Outline each uninfected red blood cell.
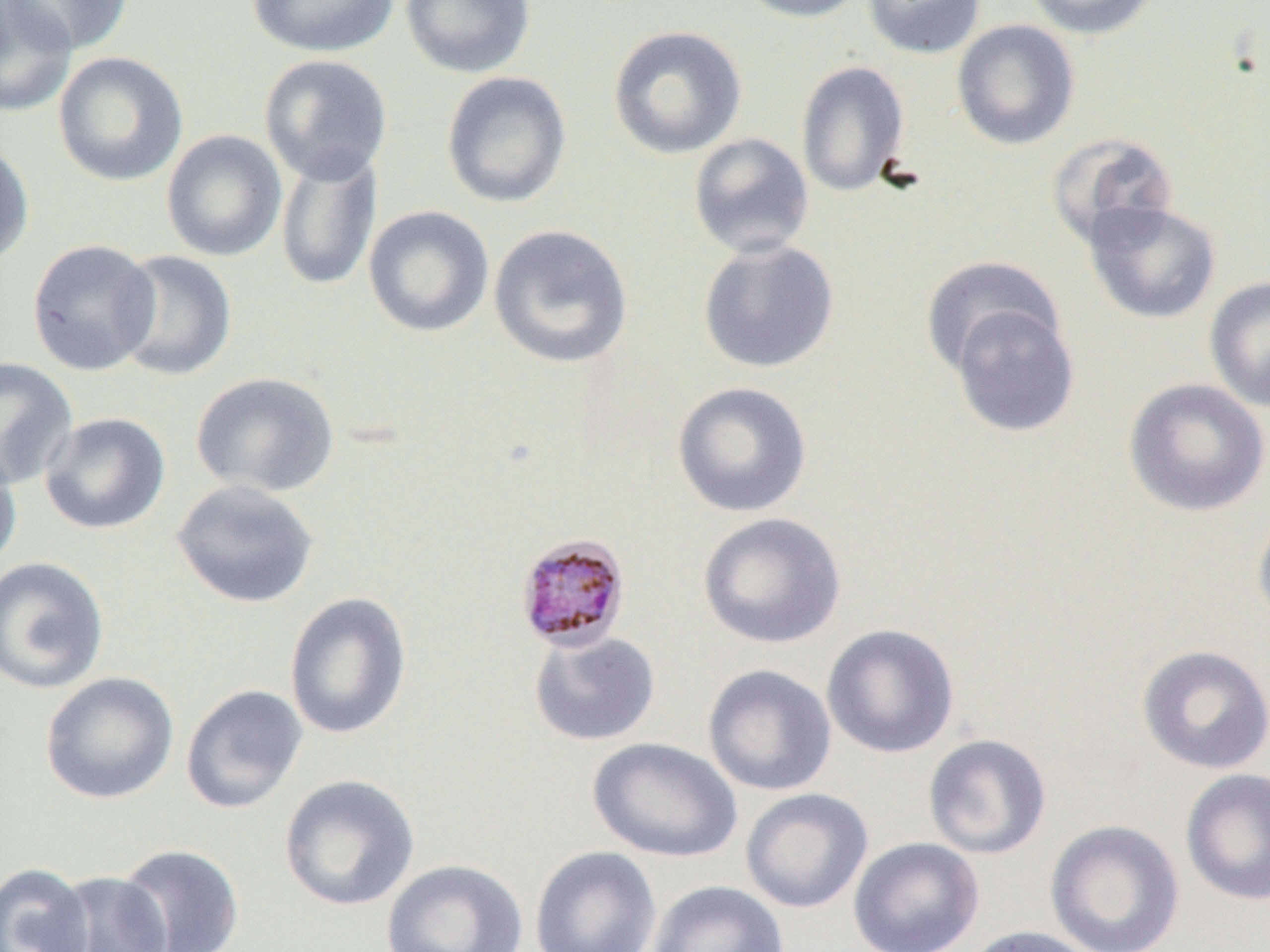

Approximate bounding boxes as (x1, y1, x2, y2) in pixels.
Uninfected red blood cells: (0, 0, 77, 118), (4, 0, 134, 56), (246, 0, 399, 58), (400, 0, 535, 79), (732, 0, 872, 23), (863, 0, 986, 59), (1023, 0, 1161, 40), (951, 19, 1080, 151), (607, 25, 747, 160), (53, 51, 188, 187), (258, 54, 393, 186), (795, 60, 910, 198), (441, 71, 571, 208), (161, 129, 288, 262), (687, 132, 814, 258), (1046, 133, 1179, 250), (0, 138, 34, 268), (275, 149, 382, 292), (1083, 200, 1221, 324), (363, 205, 494, 338), (488, 223, 633, 369), (697, 238, 839, 374), (27, 239, 159, 375), (112, 250, 237, 381), (920, 254, 1063, 380), (1204, 275, 1270, 412), (944, 298, 1080, 438), (0, 357, 78, 491), (190, 371, 339, 498), (1123, 377, 1269, 518), (671, 381, 812, 518), (39, 412, 170, 535), (0, 447, 22, 573), (171, 479, 319, 608), (1253, 506, 1270, 631), (697, 512, 846, 649), (0, 556, 109, 695), (283, 592, 412, 740), (821, 623, 960, 759), (528, 630, 661, 746), (1135, 644, 1270, 775), (702, 663, 837, 797), (39, 671, 179, 804), (180, 684, 308, 814), (923, 733, 1051, 860), (588, 737, 741, 863), (1180, 768, 1270, 906), (278, 774, 420, 911), (740, 788, 873, 913), (1045, 819, 1185, 952), (848, 837, 984, 952), (116, 843, 245, 951), (529, 845, 661, 952), (381, 859, 528, 952), (0, 862, 94, 951), (47, 870, 173, 952), (647, 880, 789, 952), (960, 925, 1101, 952).

Summary:
  - Plasmodium malariae-infected red blood cell locations: (513, 533, 631, 653)
  - Slide-level diagnosis: Plasmodium malariae
  - Preparation: thin blood film
  - Modality: light microscopy
  - Image size: 1270×952 pixels
  - Magnification: 1000x
  - Field of view: one of a larger specimen